Report the malaria status of this cell.
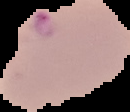

Parasitized.

preparation: thin blood smear
image_size: 130×112 pixels
image_type: cell region segmented out of the field of view; surrounding area masked to black